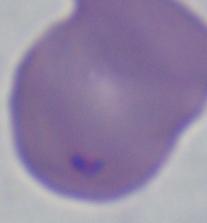
Summary:
  - Identification: Babesia
  - Magnification: 1000x
  - Modality: micrograph